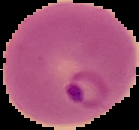

Image is 139×130 pixels. Malaria status: parasitized. The area outside the segmented cell region is set to black. From a thin blood film.